Give the position of every leukocyte visible.
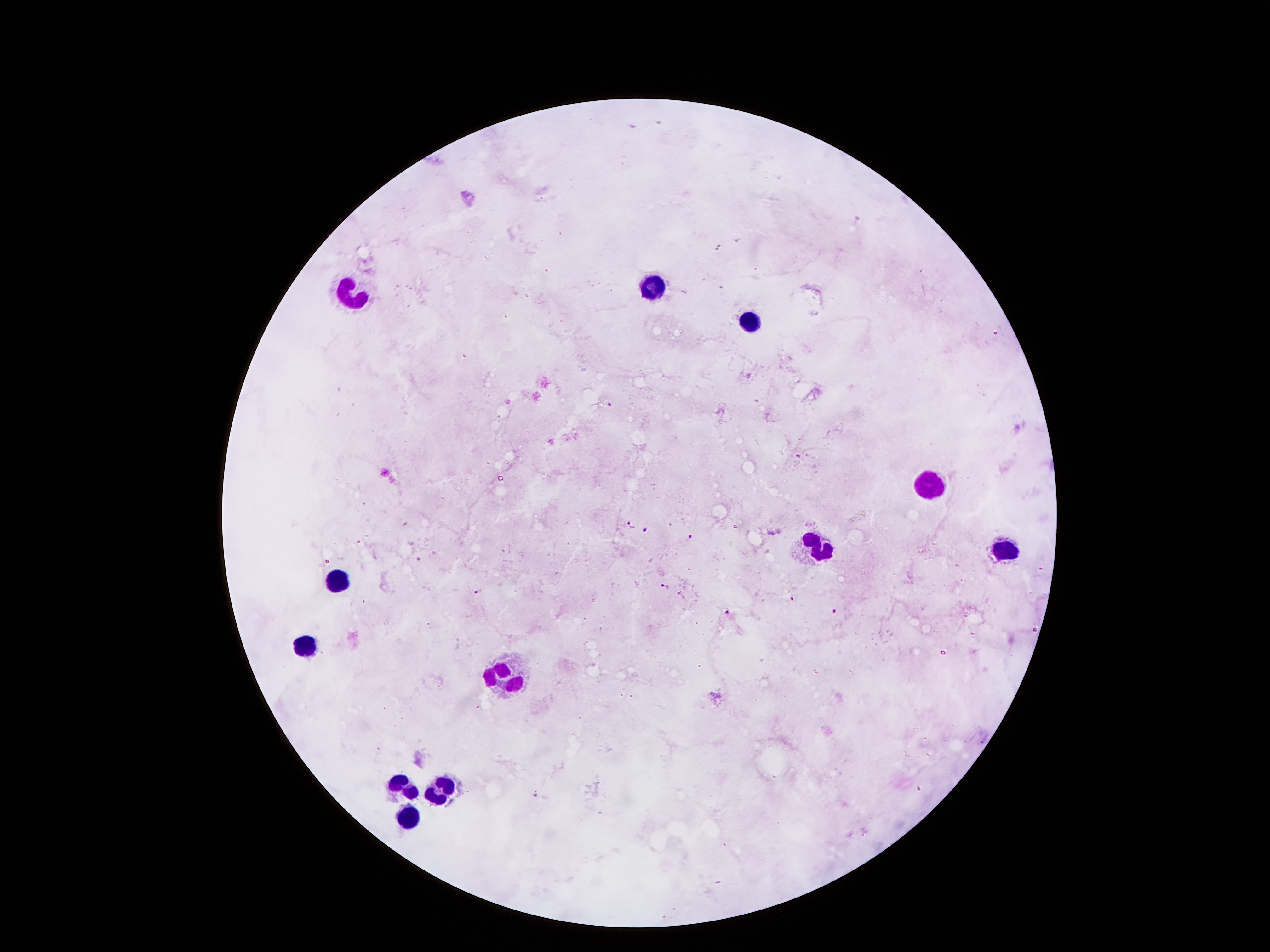

Approximate object centers, in pixels from the top-left corner.
Leukocytes: (x=651, y=290), (x=345, y=299), (x=747, y=324), (x=933, y=484), (x=813, y=548), (x=1007, y=550), (x=329, y=578), (x=303, y=650), (x=507, y=678), (x=445, y=788), (x=401, y=790), (x=409, y=814).

malaria parasite locations = (x=608, y=404), (x=801, y=456), (x=629, y=523), (x=647, y=530), (x=692, y=539), (x=419, y=558), (x=663, y=587), (x=479, y=590), (x=790, y=598), (x=833, y=609), (x=726, y=613), (x=536, y=796)
image size = 1270×952 pixels
field of view = single
patient malaria status = positive for Plasmodium falciparum
stain = Giemsa
capture = smartphone through the microscope eyepiece
preparation = thick peripheral-blood smear
magnification = 100x